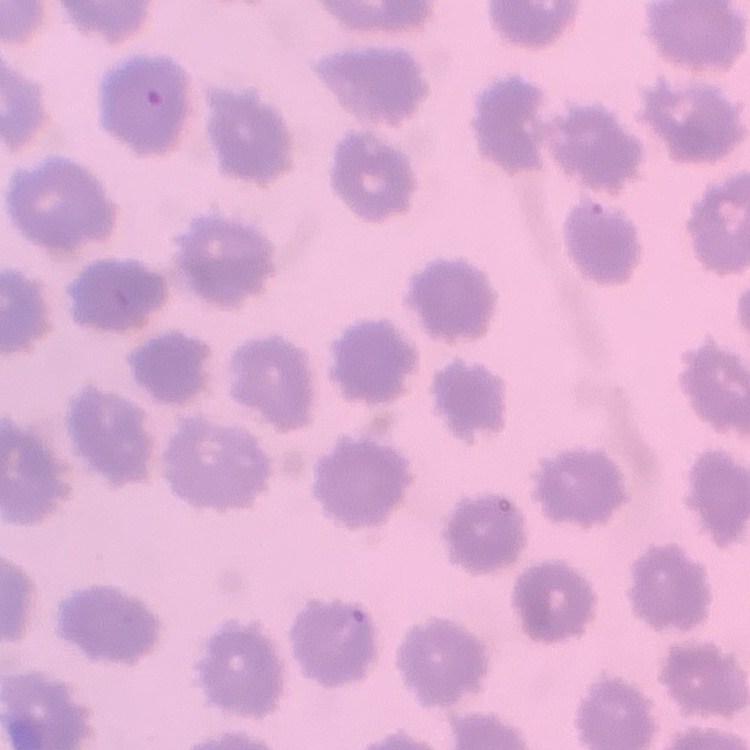 The erythrocytes exhibit no rouleaux formation. Stained with either Field's or Giemsa. Thin blood film. Square crop of a larger photomicrograph.